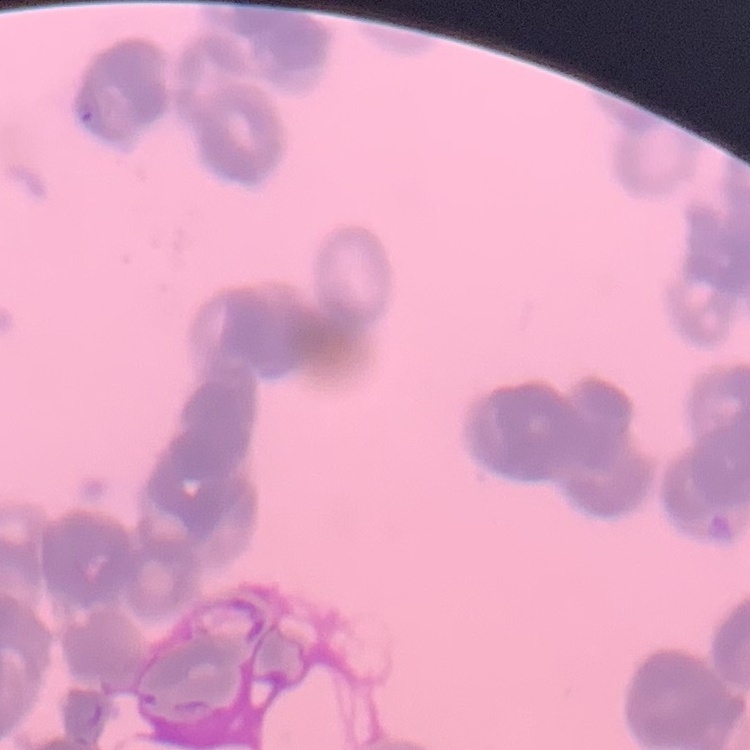
Summary:
  - Red blood cell morphology: rouleaux formation
  - Preparation: thin peripheral smear
  - Stain: Field's or Giemsa
  - Image type: one tile cut from a larger photomicrograph